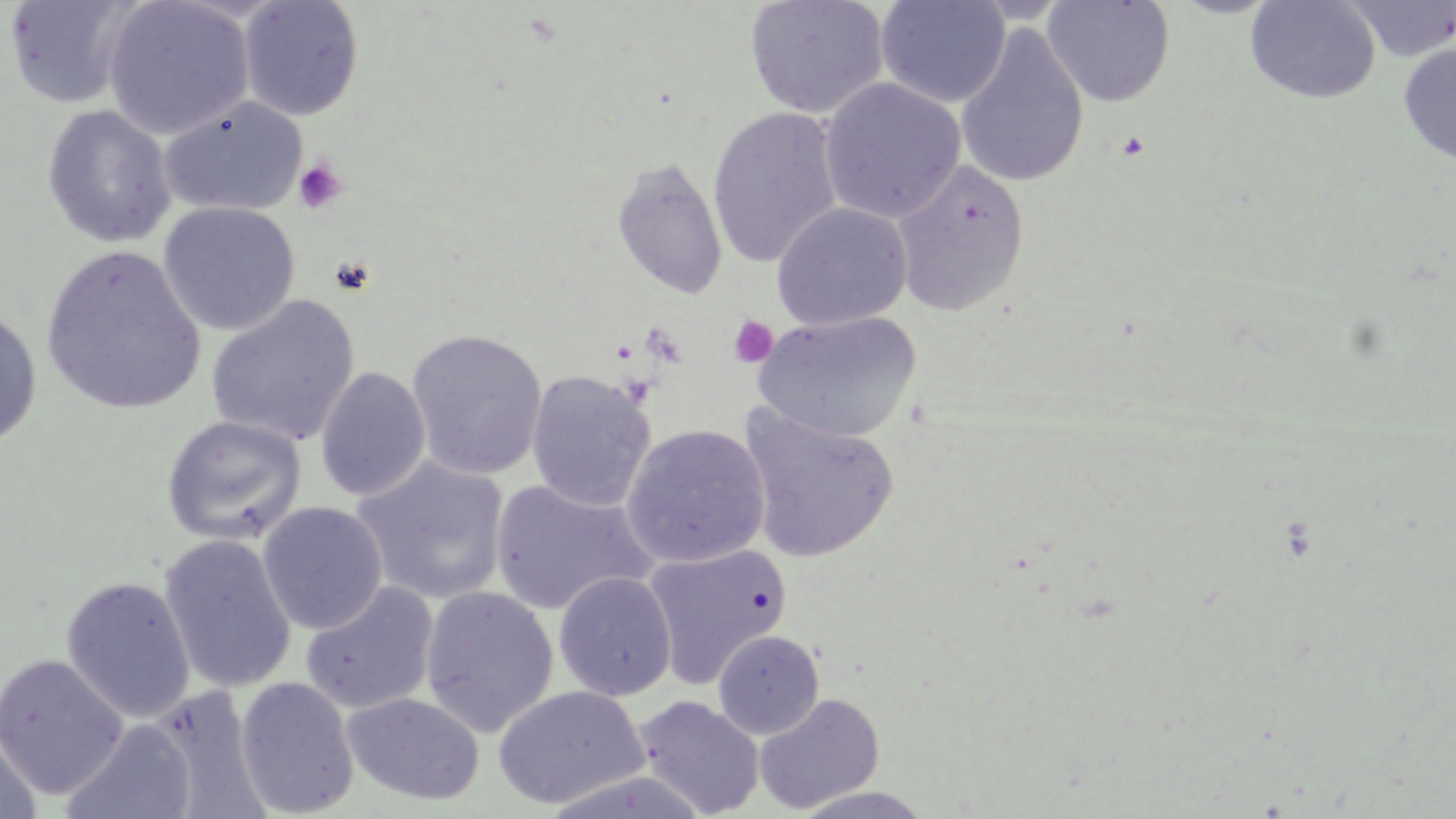
Summary:
  - Coordinate format: approximate bounding boxes as named x1/y1/x2/y2 corners in pixels
  - Uninfected red blood cell locations: (x1=3, y1=0, x2=145, y2=110), (x1=101, y1=0, x2=255, y2=140), (x1=744, y1=0, x2=889, y2=120), (x1=875, y1=0, x2=1011, y2=108), (x1=1042, y1=0, x2=1175, y2=108), (x1=1244, y1=0, x2=1381, y2=104), (x1=1343, y1=0, x2=1456, y2=61), (x1=238, y1=1, x2=365, y2=121), (x1=954, y1=24, x2=1089, y2=190), (x1=1397, y1=43, x2=1456, y2=165), (x1=819, y1=77, x2=966, y2=224), (x1=159, y1=96, x2=307, y2=217), (x1=41, y1=105, x2=177, y2=248), (x1=707, y1=107, x2=843, y2=269), (x1=610, y1=156, x2=728, y2=299), (x1=889, y1=158, x2=1031, y2=318), (x1=158, y1=202, x2=300, y2=335), (x1=771, y1=202, x2=913, y2=331), (x1=39, y1=245, x2=205, y2=415), (x1=205, y1=295, x2=361, y2=447), (x1=0, y1=306, x2=42, y2=448), (x1=752, y1=310, x2=922, y2=443), (x1=405, y1=328, x2=548, y2=481), (x1=314, y1=366, x2=431, y2=502), (x1=525, y1=370, x2=655, y2=513), (x1=737, y1=404, x2=899, y2=565), (x1=161, y1=415, x2=307, y2=546), (x1=621, y1=424, x2=771, y2=568), (x1=351, y1=456, x2=510, y2=605), (x1=489, y1=479, x2=657, y2=615), (x1=257, y1=502, x2=388, y2=635), (x1=157, y1=534, x2=298, y2=695), (x1=641, y1=544, x2=791, y2=689), (x1=553, y1=571, x2=677, y2=701), (x1=60, y1=576, x2=196, y2=723), (x1=299, y1=580, x2=439, y2=714), (x1=419, y1=585, x2=559, y2=737), (x1=712, y1=630, x2=824, y2=739), (x1=0, y1=653, x2=129, y2=801), (x1=234, y1=676, x2=359, y2=817), (x1=491, y1=684, x2=648, y2=810), (x1=662, y1=684, x2=853, y2=809), (x1=342, y1=691, x2=484, y2=806), (x1=753, y1=692, x2=885, y2=814), (x1=634, y1=695, x2=765, y2=817), (x1=60, y1=719, x2=197, y2=819), (x1=0, y1=728, x2=42, y2=818), (x1=788, y1=786, x2=937, y2=819)
  - Platelet locations: (x1=292, y1=158, x2=348, y2=216), (x1=330, y1=257, x2=376, y2=295), (x1=727, y1=315, x2=779, y2=368), (x1=642, y1=320, x2=690, y2=366)
  - Slide-level diagnosis: negative for blood parasites
  - Preparation: thin blood smear
  - Magnification: 1000x
  - Field of view: one of a larger specimen
  - Image size: 1456×819 pixels
  - Modality: light microscopy
  - Stain: May-Grünwald-Giemsa